Outline each Plasmodium vivax-infected red blood cell.
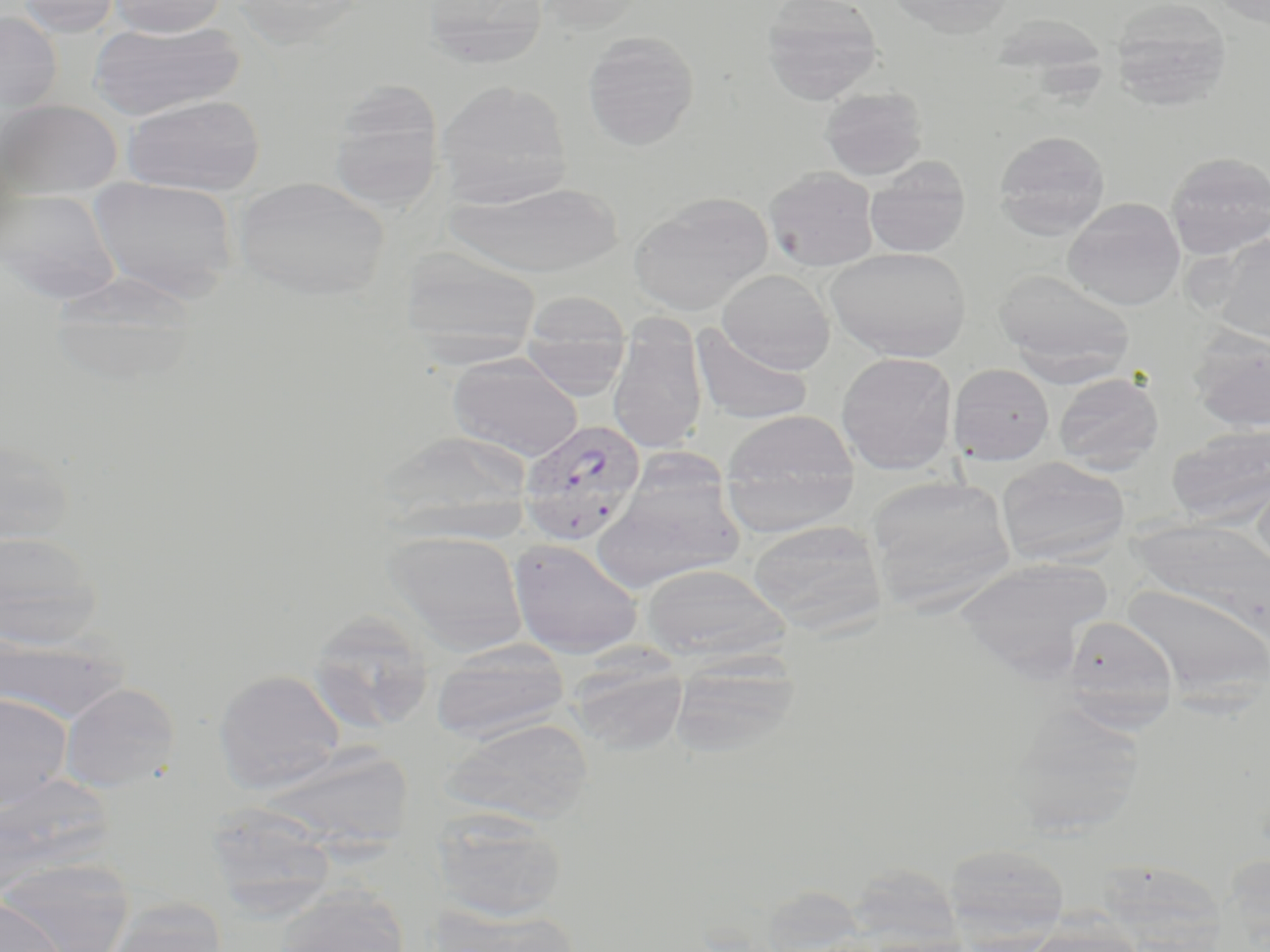

Approximate bounding boxes as named x1/y1/x2/y2 corners in pixels.
Plasmodium vivax-infected red blood cells: (x1=518, y1=418, x2=646, y2=547).

Summary:
  - Uninfected red blood cell locations: (x1=16, y1=0, x2=121, y2=37), (x1=106, y1=0, x2=229, y2=37), (x1=420, y1=0, x2=550, y2=70), (x1=534, y1=0, x2=646, y2=33), (x1=760, y1=0, x2=884, y2=103), (x1=886, y1=0, x2=1017, y2=36), (x1=1109, y1=0, x2=1233, y2=110), (x1=0, y1=11, x2=62, y2=114), (x1=89, y1=20, x2=245, y2=120), (x1=582, y1=31, x2=700, y2=151), (x1=435, y1=79, x2=572, y2=208), (x1=328, y1=82, x2=446, y2=213), (x1=820, y1=86, x2=928, y2=180), (x1=122, y1=94, x2=265, y2=196), (x1=0, y1=100, x2=122, y2=200), (x1=993, y1=130, x2=1111, y2=238), (x1=1165, y1=152, x2=1270, y2=259), (x1=864, y1=159, x2=970, y2=259), (x1=764, y1=166, x2=880, y2=271), (x1=88, y1=177, x2=239, y2=302), (x1=233, y1=177, x2=390, y2=300), (x1=444, y1=181, x2=623, y2=278), (x1=0, y1=187, x2=122, y2=304), (x1=629, y1=192, x2=773, y2=315), (x1=1063, y1=197, x2=1186, y2=311), (x1=1209, y1=235, x2=1270, y2=343), (x1=826, y1=246, x2=971, y2=362), (x1=400, y1=248, x2=542, y2=363), (x1=995, y1=267, x2=1136, y2=381), (x1=716, y1=269, x2=835, y2=373), (x1=47, y1=272, x2=202, y2=387), (x1=520, y1=292, x2=634, y2=367), (x1=607, y1=317, x2=708, y2=455), (x1=520, y1=321, x2=631, y2=403), (x1=690, y1=323, x2=813, y2=425), (x1=1188, y1=326, x2=1270, y2=433), (x1=836, y1=351, x2=958, y2=474), (x1=448, y1=353, x2=584, y2=461), (x1=948, y1=364, x2=1055, y2=465), (x1=1053, y1=373, x2=1164, y2=473), (x1=719, y1=409, x2=860, y2=535), (x1=1167, y1=424, x2=1270, y2=527), (x1=373, y1=430, x2=534, y2=543), (x1=0, y1=436, x2=77, y2=548), (x1=997, y1=457, x2=1130, y2=566), (x1=1251, y1=465, x2=1270, y2=575), (x1=595, y1=473, x2=744, y2=593), (x1=864, y1=474, x2=1019, y2=614), (x1=1131, y1=517, x2=1270, y2=629), (x1=746, y1=519, x2=888, y2=635), (x1=0, y1=530, x2=102, y2=649), (x1=384, y1=530, x2=528, y2=653), (x1=508, y1=538, x2=644, y2=659), (x1=955, y1=557, x2=1110, y2=675), (x1=640, y1=564, x2=791, y2=665), (x1=1118, y1=582, x2=1270, y2=705), (x1=305, y1=609, x2=435, y2=734), (x1=1062, y1=615, x2=1181, y2=726), (x1=0, y1=630, x2=128, y2=726), (x1=430, y1=639, x2=570, y2=743), (x1=566, y1=653, x2=689, y2=756), (x1=669, y1=655, x2=802, y2=759), (x1=213, y1=669, x2=346, y2=792), (x1=58, y1=682, x2=181, y2=793), (x1=0, y1=694, x2=73, y2=812), (x1=1005, y1=705, x2=1146, y2=838), (x1=441, y1=718, x2=593, y2=826), (x1=263, y1=743, x2=414, y2=852), (x1=0, y1=772, x2=114, y2=898), (x1=204, y1=802, x2=338, y2=914), (x1=431, y1=808, x2=568, y2=923), (x1=942, y1=842, x2=1071, y2=948), (x1=1095, y1=857, x2=1230, y2=951), (x1=1, y1=861, x2=132, y2=952), (x1=843, y1=862, x2=965, y2=950), (x1=272, y1=886, x2=412, y2=952), (x1=0, y1=896, x2=66, y2=952), (x1=99, y1=900, x2=229, y2=952), (x1=431, y1=904, x2=580, y2=952)
  - Slide-level diagnosis: Plasmodium vivax
  - Modality: optical microscopy
  - Field of view: one of a larger specimen
  - Magnification: 1000x
  - Image size: 1270×952 pixels
  - Stain: May-Grünwald-Giemsa
  - Preparation: thin blood smear